Report the malaria status of this cell.
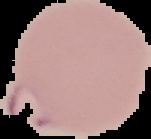

It is parasitized.

{
  "preparation": "thin blood smear",
  "image_type": "segmented cell region with the area outside set to black",
  "image_size": "151×139 pixels"
}